Name the cell type shown.
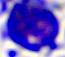
This is a leukocyte.

magnification: 400x
modality: photomicrograph